Classify this cell by malaria status.
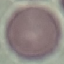

It is uninfected.

Giemsa stain. Cell patch, automatically extracted from a larger field of view and resized to 64 × 64 pixels. Thin blood smear. Photographed with a smartphone camera at the microscope eyepiece.